State the blood parasite species.
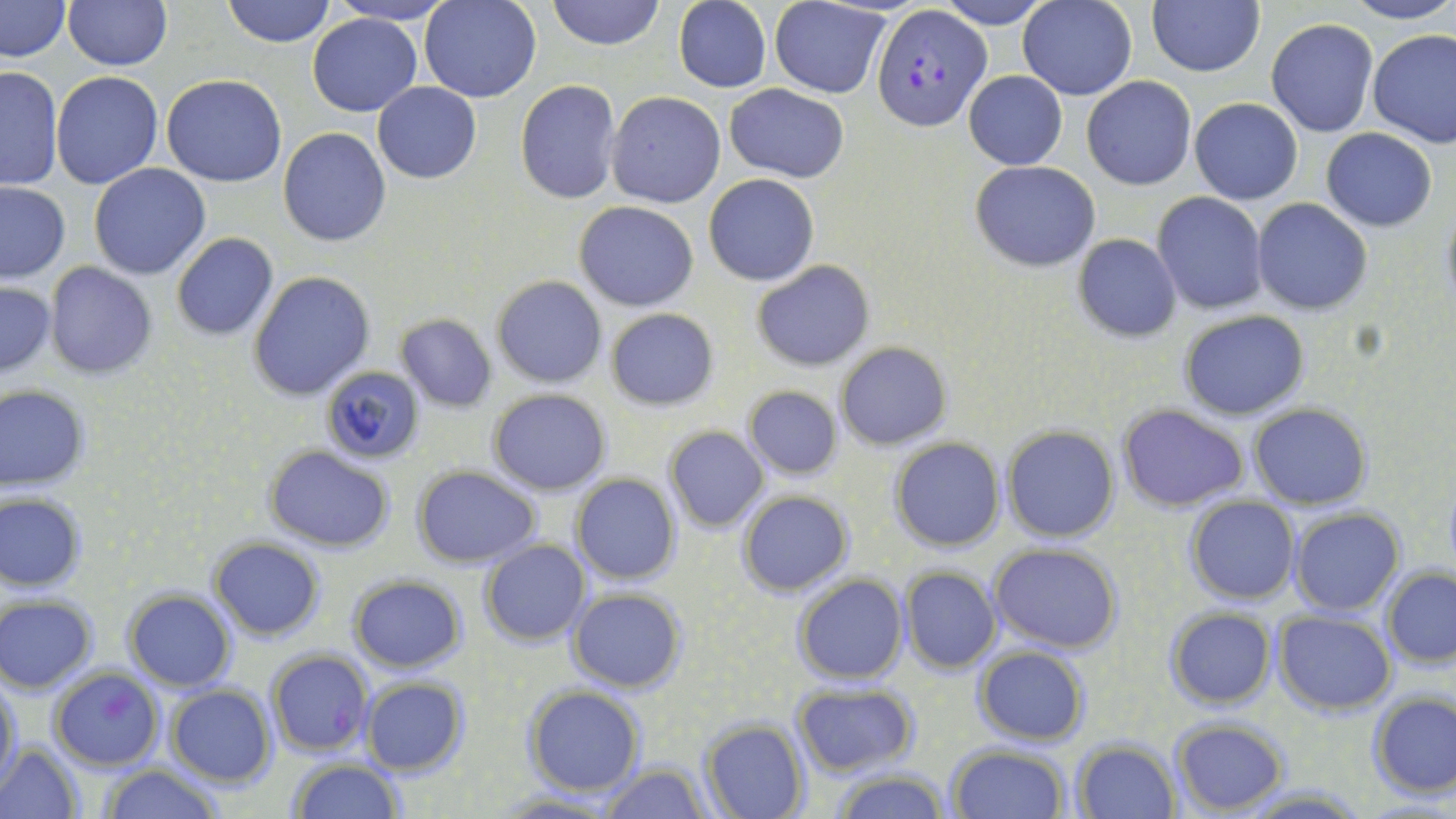

Plasmodium falciparum.

stain = May-Grünwald-Giemsa
Plasmodium falciparum-infected red blood cell locations = approximate bounding boxes as (x1,y1)-(x2,y2) corner pairs in pixels: (871,6)-(992,132), (266,651)-(374,755), (48,668)-(164,772)
image size = 1456×819 pixels
magnification = 1000x
field of view = single
preparation = thin blood smear
modality = light microscopy
uninfected red blood cell locations = approximate bounding boxes as (x1,y1)-(x2,y2) corner pairs in pixels: (1,0)-(71,62), (222,0)-(335,48), (328,0)-(460,26), (420,0)-(542,103), (547,0)-(664,50), (934,0)-(1055,29), (1147,0)-(1265,77), (1341,0)-(1456,25), (64,1)-(171,71), (674,1)-(772,92), (769,1)-(891,97), (1017,1)-(1137,101), (306,12)-(421,117), (1266,19)-(1379,137), (1367,29)-(1456,147), (0,66)-(63,191), (51,71)-(161,190), (964,71)-(1068,170), (162,75)-(287,187), (1081,77)-(1197,189), (515,80)-(622,204), (372,82)-(482,183), (724,85)-(850,181), (606,92)-(726,207), (1189,98)-(1304,204), (278,128)-(392,246), (1322,128)-(1437,232), (971,161)-(1100,271), (89,164)-(211,280), (704,173)-(820,286), (1,181)-(69,281), (1153,192)-(1269,315), (1439,198)-(1456,315), (1253,199)-(1372,315), (574,202)-(699,312), (172,234)-(278,340), (1073,234)-(1180,342), (752,261)-(875,369), (45,263)-(157,380), (249,272)-(374,399), (493,275)-(607,388), (0,281)-(55,378), (606,308)-(719,410), (1178,309)-(1310,420), (396,313)-(497,412), (835,342)-(951,449), (319,368)-(425,465), (0,385)-(90,491), (743,386)-(843,480), (488,388)-(612,495), (1119,404)-(1249,512), (1248,404)-(1372,510), (663,426)-(769,533), (1003,426)-(1119,543), (890,439)-(1004,552), (263,444)-(395,551), (412,465)-(542,568), (571,473)-(681,587), (736,490)-(853,597), (1,492)-(86,591), (1185,496)-(1300,604), (1289,508)-(1403,617), (208,537)-(324,639), (480,540)-(589,646), (990,544)-(1124,652), (900,568)-(1002,673), (1382,568)-(1456,666), (794,573)-(909,684), (349,575)-(466,672), (567,587)-(688,694), (123,589)-(235,691), (0,595)-(98,693), (1163,608)-(1276,710), (1273,611)-(1394,712), (973,646)-(1089,745), (360,676)-(469,776), (1,681)-(20,792), (521,683)-(646,797), (791,683)-(919,776), (166,685)-(276,787), (1367,691)-(1456,798), (1168,718)-(1290,815), (701,721)-(807,819), (1071,740)-(1181,819), (946,741)-(1072,819), (0,742)-(83,818), (285,757)-(404,819), (598,763)-(711,819), (99,764)-(222,819), (830,767)-(950,819), (1237,783)-(1370,816), (493,792)-(628,818)